Identify the cell.
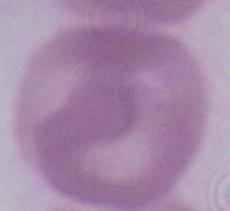

This is an erythrocyte.

{
  "magnification": "1000x",
  "modality": "photomicrograph"
}